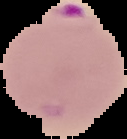

Summary:
  - Preparation: thin blood smear
  - Result: malaria parasites detected
  - Image type: cell region segmented out of the field of view; surrounding area masked to black
  - Image size: 127×139 pixels